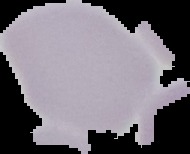

malaria status = uninfected
preparation = thin blood smear
image type = segmented cell region with the area outside set to black
image size = 190×154 pixels